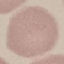
Result: no malaria parasites detected. Automatically extracted cell patch, resized to 64 × 64 pixels. Thin blood smear. Giemsa stain. Acquired by smartphone through the microscope eyepiece.